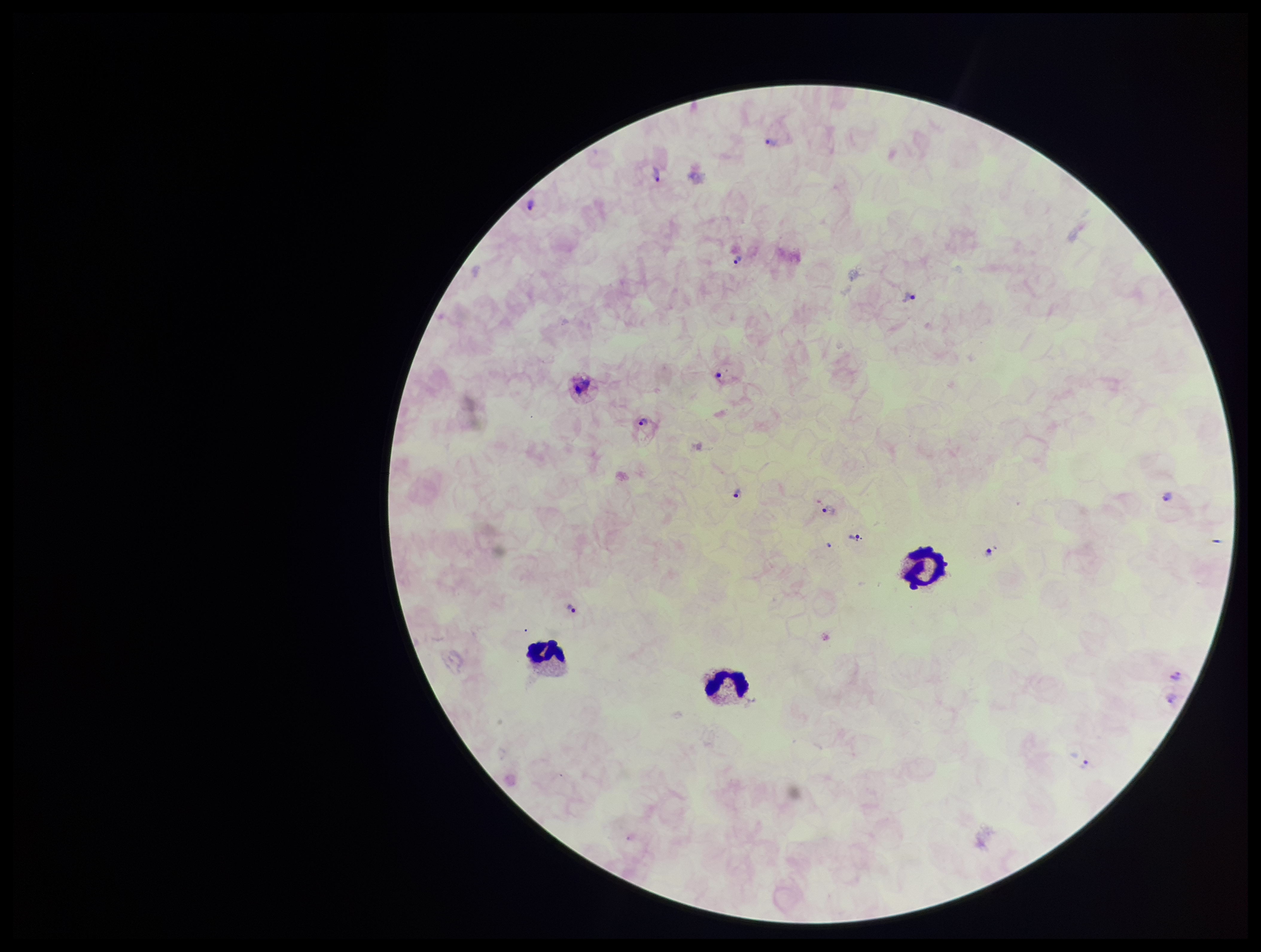
preparation = thick blood smear
stain = Giemsa
patient malaria status = positive
parasite count = 14
Plasmodium parasites = identified
field of view = single
leukocyte count = 3
species reported for this patient = Plasmodium vivax
image size = 1261×952 pixels
capture = smartphone photograph through the microscope eyepiece